Assess the morphology of the erythrocytes.
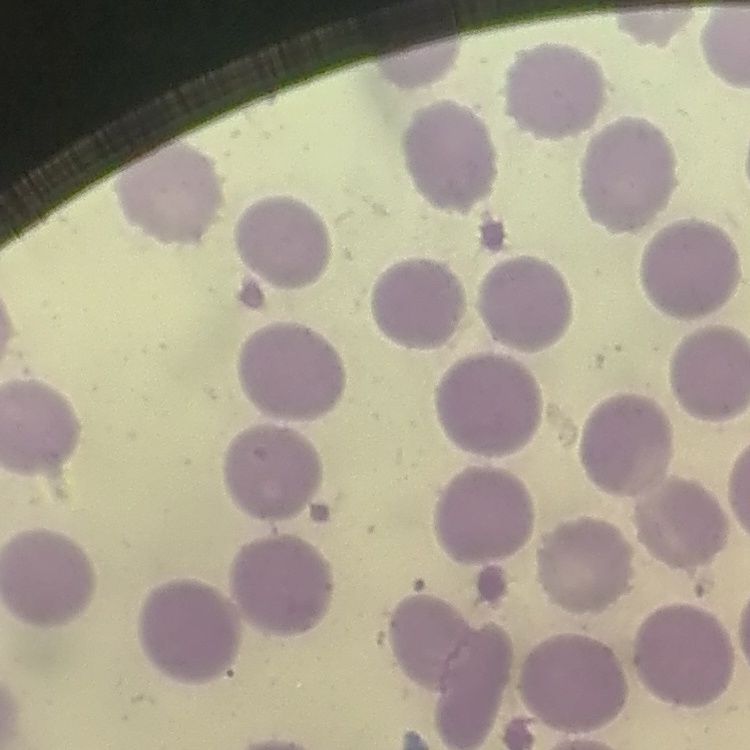

No rouleaux formation.

Thin blood smear. One tile cut from a larger photomicrograph. Field's or Giemsa stain.